Identify the parasite.
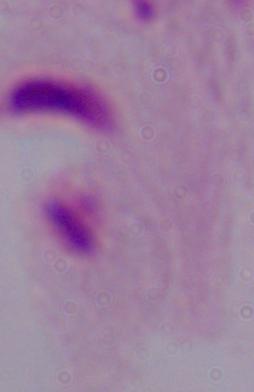

This is a trichomonad.

magnification = 1000x
modality = micrograph